Describe the morphology of the red blood cells.
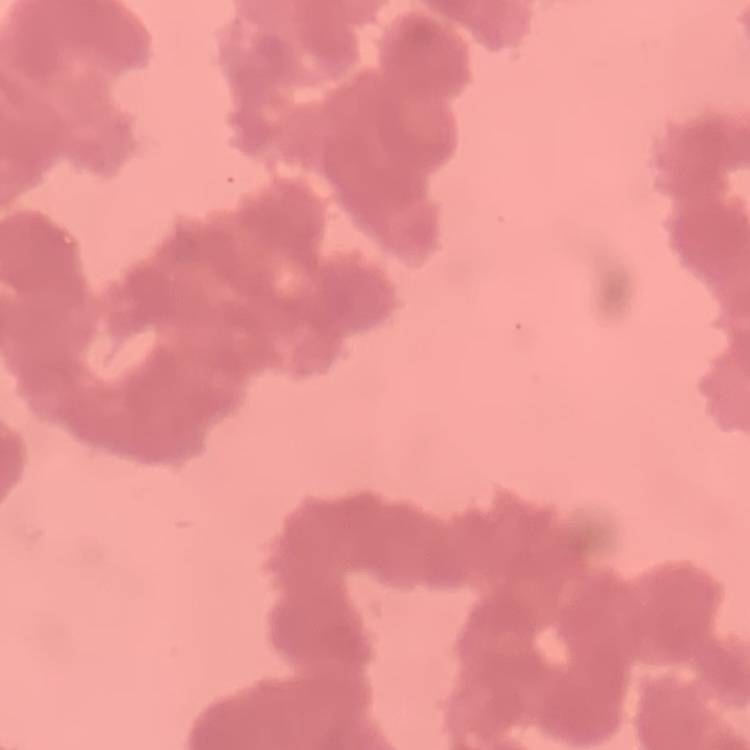

Rouleaux formation.

Summary:
  - Image type: one tile cut from a larger photomicrograph
  - Stain: Field's or Giemsa
  - Preparation: thin blood film